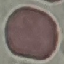
malaria_status: uninfected
preparation: thin blood film
image_type: cell patch, automatically extracted from a larger field of view and resized to 64 × 64 pixels
stain: Giemsa
capture: smartphone camera at the microscope eyepiece